Comment on the morphology of the erythrocytes.
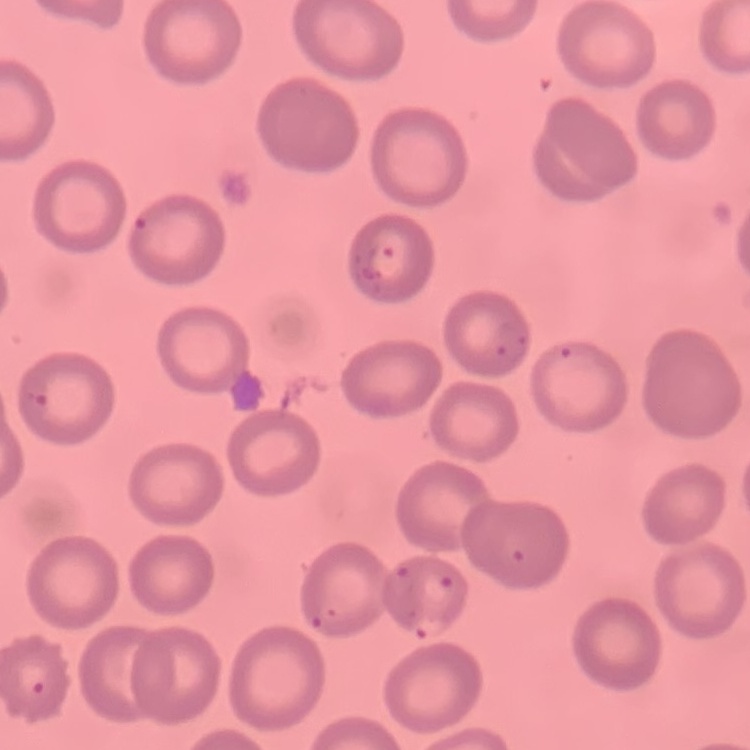

No rouleaux formation.

Summary:
  - Preparation: thin blood smear
  - Stain: Field's or Giemsa
  - Image type: one tile cut from a larger photomicrograph